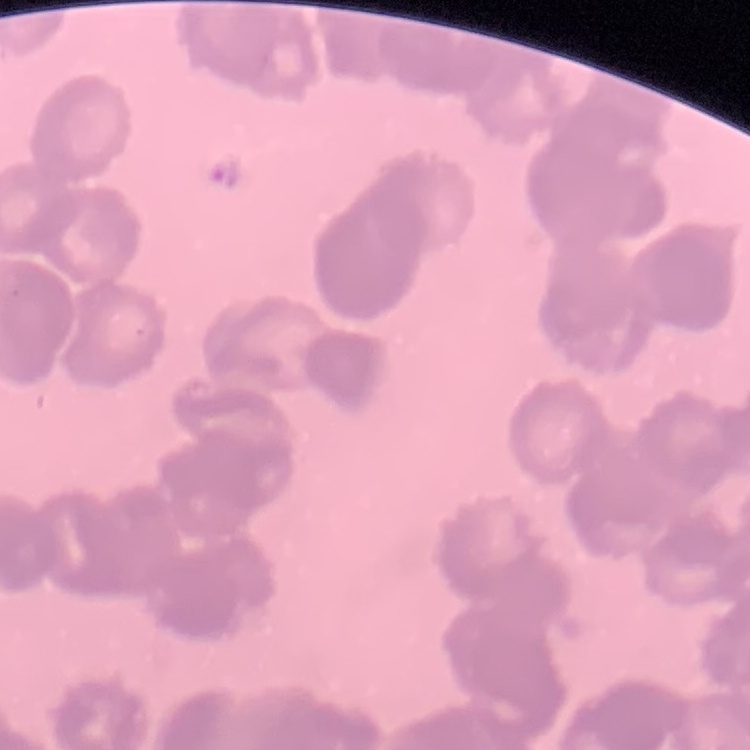
erythrocyte morphology = rouleaux formation
image type = square crop of a larger photomicrograph
stain = Field's or Giemsa
preparation = thin blood film